Assess this cell for malaria.
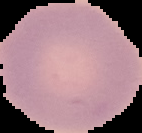

It is uninfected.

image type = segmented cell region on a black background
image size = 142×133 pixels
preparation = thin blood smear